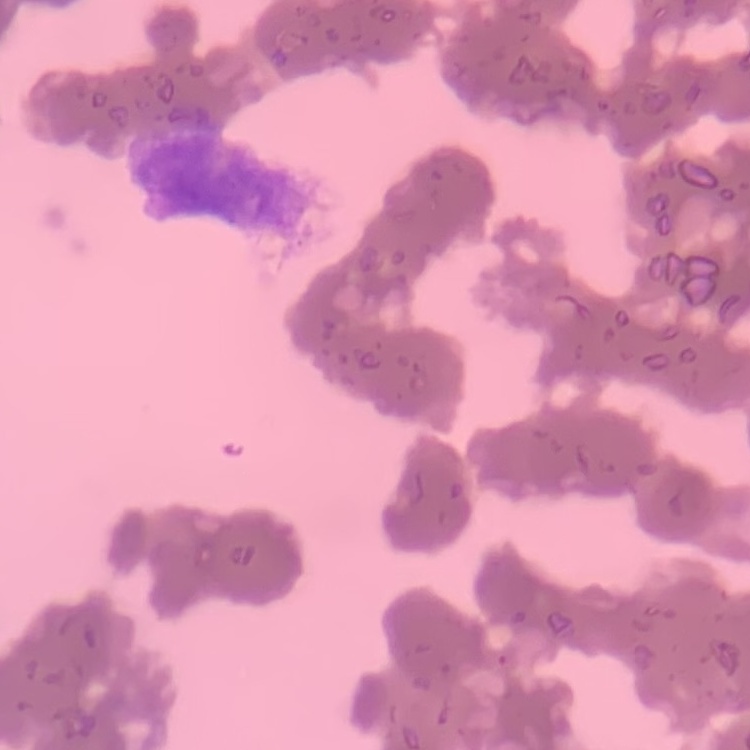
red blood cell morphology = rouleaux formation
stain = Field's or Giemsa
image type = one tile cut from a larger photomicrograph
preparation = thin peripheral smear